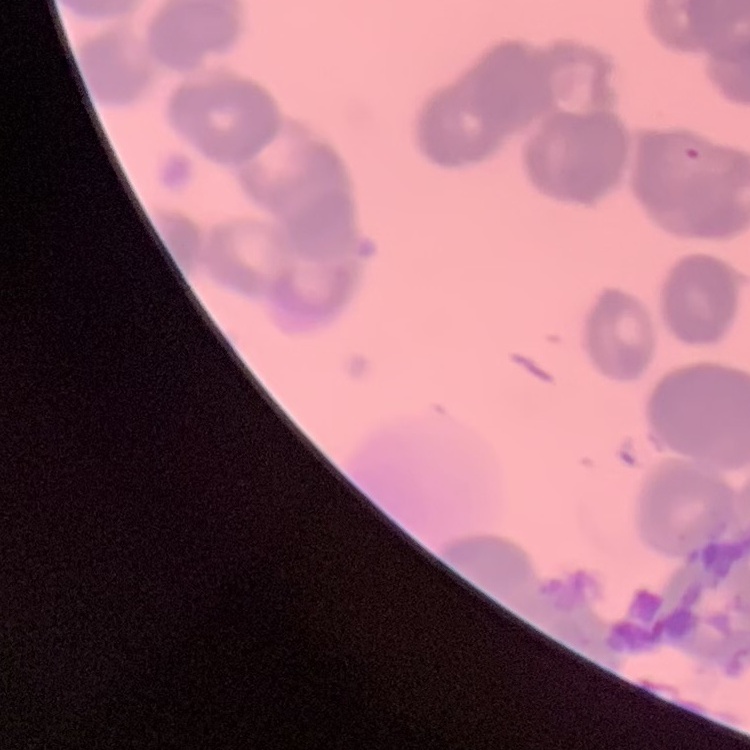
Summary:
  - Red blood cell morphology: rouleaux formation
  - Image type: one tile cut from a larger photomicrograph
  - Stain: Field's or Giemsa
  - Preparation: thin peripheral smear